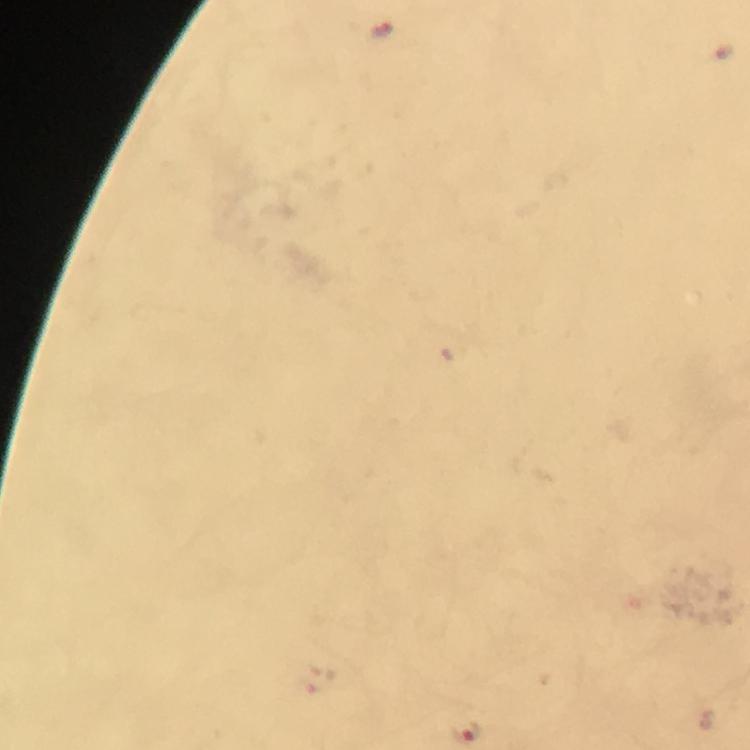 Approximate centers as [x, y] in pixels. Malaria parasite locations: [382, 30], [466, 732]. Thick smear. Immersion oil was used. From a malaria diagnostic workup. At 100x magnification. Cropped region of a single field of view. Photographed with a smartphone mounted on the microscope. Giemsa stain. Image is 750×750 pixels.